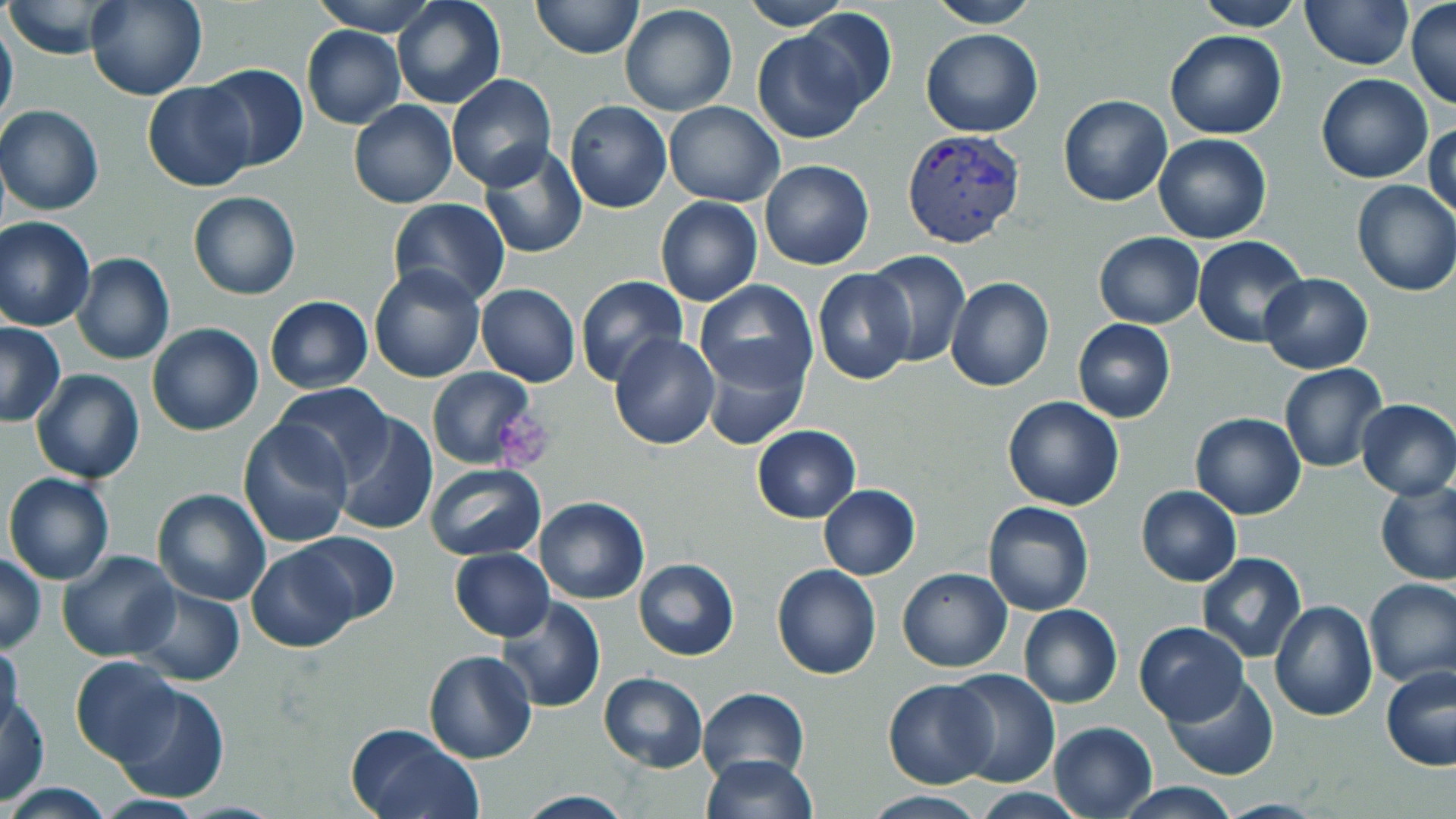 Approximate bounding boxes as (x1, y1, x2, y2) in pixels. Platelet locations: (492, 407, 555, 470). Plasmodium vivax-infected red blood cell locations: (900, 128, 1027, 248). Uninfected red blood cell locations: (5, 0, 120, 59), (85, 0, 207, 101), (309, 0, 442, 36), (391, 0, 505, 109), (530, 0, 646, 59), (738, 0, 851, 31), (926, 0, 1040, 27), (1190, 0, 1304, 31), (1405, 0, 1456, 111), (1301, 1, 1412, 71), (620, 4, 738, 115), (795, 8, 899, 116), (0, 15, 18, 136), (300, 25, 405, 129), (752, 27, 871, 144), (920, 28, 1044, 138), (1165, 30, 1286, 141), (199, 64, 308, 173), (1316, 73, 1433, 184), (445, 74, 558, 191), (143, 80, 258, 193), (1057, 94, 1174, 207), (348, 99, 457, 208), (564, 101, 672, 214), (664, 101, 784, 205), (1, 104, 104, 215), (1426, 118, 1456, 226), (1152, 133, 1271, 243), (478, 145, 589, 261), (758, 159, 874, 270), (1351, 180, 1456, 296), (188, 190, 301, 299), (656, 196, 763, 305), (387, 199, 509, 308), (0, 216, 96, 330), (1094, 232, 1203, 329), (1192, 236, 1308, 347), (864, 251, 971, 366), (72, 253, 174, 365), (369, 264, 486, 383), (813, 268, 917, 385), (1259, 274, 1372, 373), (574, 275, 687, 388), (945, 278, 1054, 392), (694, 279, 817, 394), (475, 284, 580, 386), (264, 296, 373, 392), (1073, 318, 1175, 423), (0, 322, 65, 427), (146, 323, 265, 436), (609, 332, 720, 449), (696, 341, 808, 452), (1279, 363, 1389, 473), (427, 367, 540, 470), (30, 368, 144, 483), (270, 382, 395, 486), (1002, 395, 1126, 511), (1355, 398, 1456, 499), (333, 413, 439, 534), (1191, 413, 1305, 519), (238, 420, 353, 548), (752, 425, 860, 522), (425, 463, 546, 561), (3, 473, 116, 585), (1375, 480, 1456, 586), (817, 484, 921, 580), (1135, 485, 1240, 588), (152, 488, 270, 606), (534, 497, 650, 604), (982, 501, 1094, 616), (294, 529, 398, 624), (247, 544, 359, 652), (450, 549, 554, 641), (58, 551, 182, 660), (1195, 551, 1306, 663), (1, 553, 47, 652), (633, 558, 740, 659), (771, 563, 882, 680), (897, 567, 1012, 672), (1362, 578, 1456, 688), (133, 583, 245, 686), (497, 596, 606, 713), (1269, 600, 1377, 721), (1019, 604, 1122, 709), (1134, 621, 1249, 726), (0, 640, 24, 740), (423, 649, 537, 764), (70, 656, 184, 766), (1380, 665, 1456, 771), (944, 670, 1061, 787), (597, 672, 707, 773), (1164, 674, 1278, 780), (882, 677, 999, 789), (112, 681, 230, 802), (697, 688, 810, 783), (1, 696, 49, 802), (1048, 720, 1159, 818), (345, 724, 482, 819), (698, 755, 820, 818), (5, 781, 113, 818), (1116, 783, 1240, 817), (513, 791, 639, 819), (862, 791, 991, 818). Slide-level diagnosis: Plasmodium vivax. May-Grünwald-Giemsa-stained preparation. Light microscopy. Thin blood smear. Image is 1456×819 pixels. One field of a larger specimen. Captured at 1000x magnification.